Locate and identify every blood parasite.
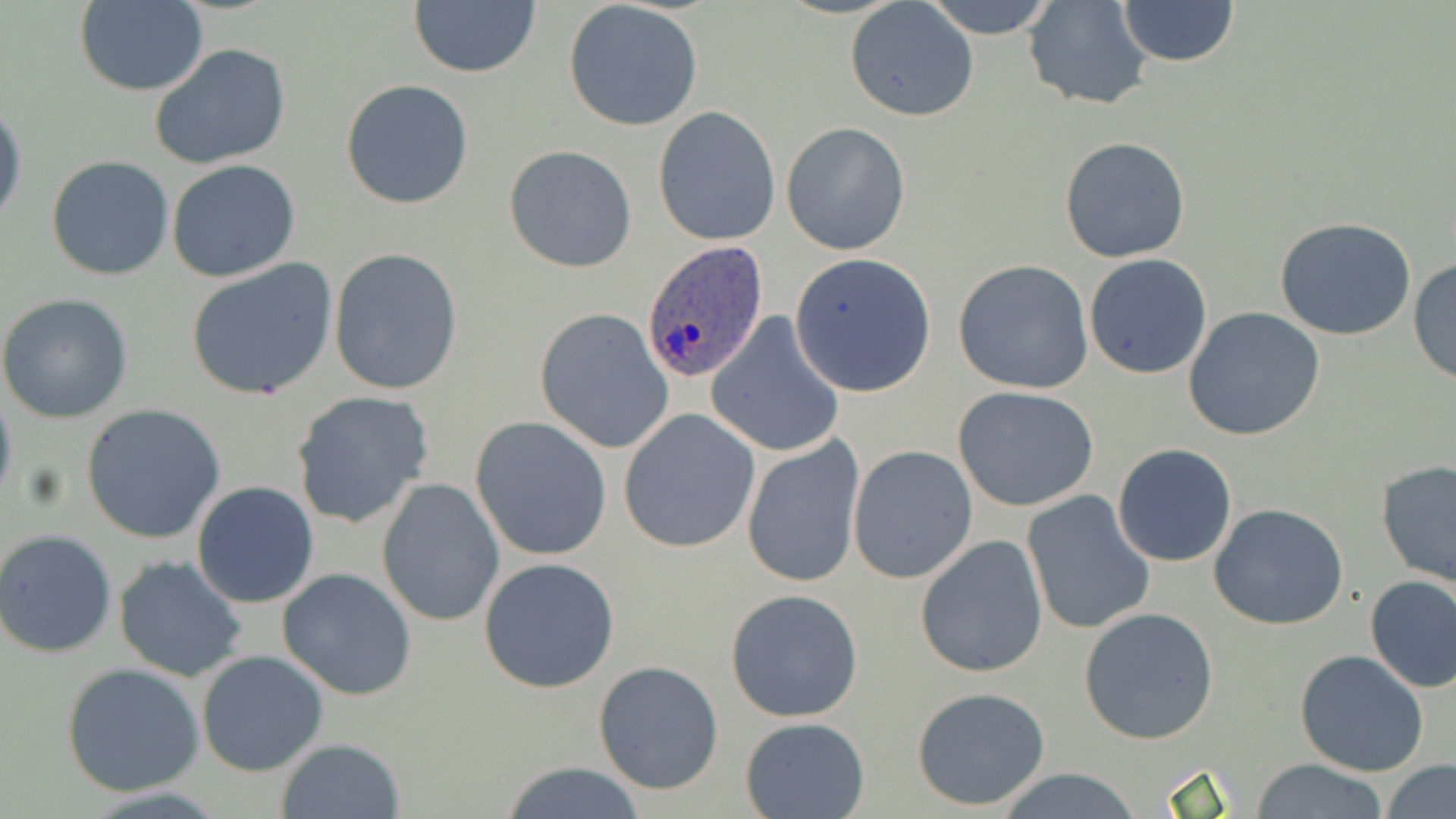
Approximate bounding boxes as (x1, y1, x2, y2) in pixels.
Plasmodium ovale-infected red blood cells: (640, 240, 770, 381).
No Plasmodium falciparum, Plasmodium malariae, Plasmodium vivax, Babesia divergens, or Trypanosoma brucei observed.

Summary:
  - Uninfected red blood cell locations: (920, 0, 1060, 39), (1021, 0, 1156, 112), (74, 1, 206, 96), (408, 1, 542, 78), (1115, 1, 1241, 68), (562, 2, 704, 131), (845, 2, 979, 123), (148, 43, 294, 172), (341, 80, 475, 209), (0, 97, 25, 233), (653, 106, 782, 247), (781, 121, 911, 253), (1058, 136, 1192, 264), (503, 145, 637, 272), (46, 155, 175, 282), (167, 160, 301, 283), (1274, 217, 1419, 342), (327, 247, 463, 396), (788, 253, 938, 398), (1084, 253, 1213, 379), (1408, 255, 1455, 385), (185, 259, 340, 400), (951, 259, 1096, 395), (0, 294, 133, 425), (1183, 306, 1325, 442), (534, 308, 675, 455), (705, 313, 846, 459), (0, 382, 18, 512), (953, 386, 1101, 513), (291, 391, 435, 530), (81, 403, 226, 544), (619, 408, 759, 553), (470, 416, 613, 561), (742, 437, 866, 588), (1112, 444, 1237, 567), (847, 445, 979, 584), (1375, 460, 1456, 588), (376, 478, 505, 627), (191, 481, 320, 609), (1021, 491, 1156, 636), (1208, 503, 1352, 630), (1, 528, 117, 657), (914, 534, 1049, 678), (113, 555, 250, 683), (478, 556, 620, 693), (278, 568, 418, 701), (1364, 575, 1456, 694), (725, 589, 864, 723), (1079, 608, 1219, 744), (1295, 649, 1429, 776), (196, 651, 329, 777), (593, 661, 725, 795), (61, 663, 205, 797), (912, 687, 1053, 812), (740, 716, 870, 819), (274, 738, 405, 819), (1251, 759, 1390, 817), (1382, 761, 1456, 819), (496, 762, 653, 818), (996, 770, 1147, 818)
  - Slide-level diagnosis: Plasmodium ovale
  - Preparation: thin blood smear
  - Modality: light microscopy
  - Field of view: one of a larger specimen
  - Image size: 1456×819 pixels
  - Stain: May-Grünwald-Giemsa
  - Magnification: 1000x